Assess the morphology of the red blood cells.
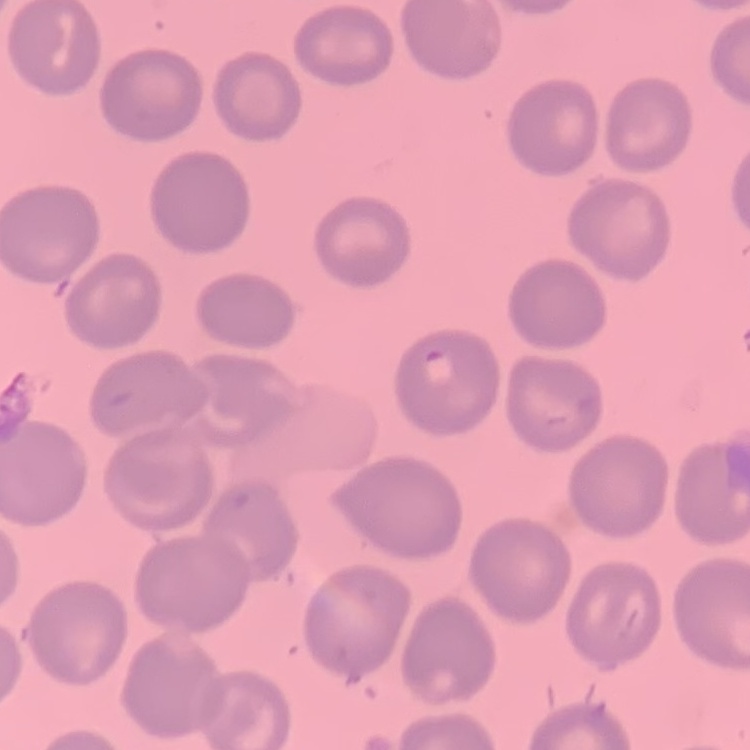
No rouleaux formation.

Thin blood smear. Stained with either Field's or Giemsa. Square crop of a larger photomicrograph.